Identify the blood parasite species.
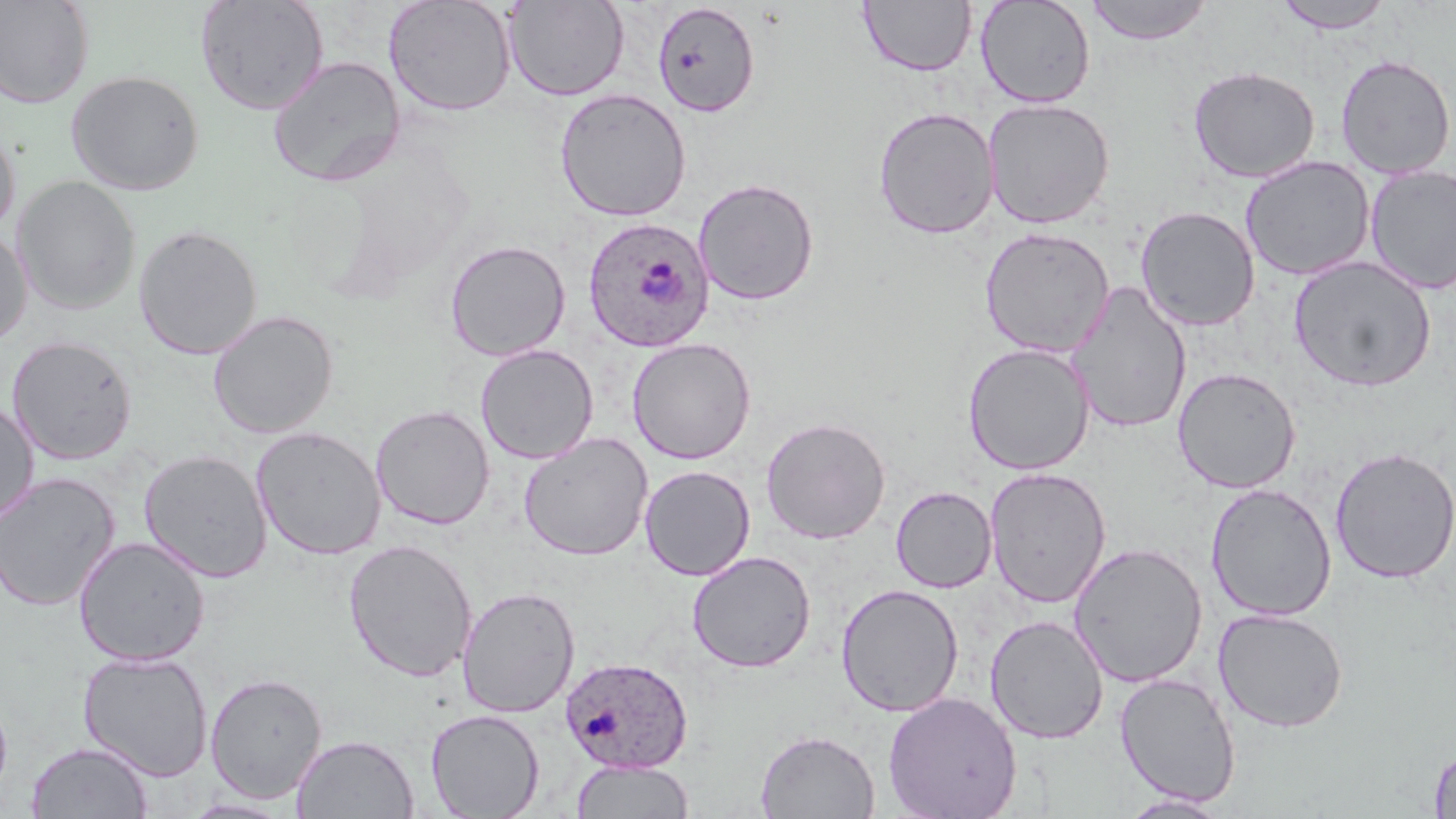
Plasmodium ovale.

Summary:
  - Coordinate format: approximate bounding boxes as (x1, y1, x2, y2) in pixels
  - Plasmodium ovale-infected red blood cell locations: (582, 216, 715, 352), (559, 655, 694, 773)
  - Uninfected red blood cell locations: (0, 0, 95, 109), (195, 0, 329, 115), (384, 0, 516, 118), (976, 0, 1096, 108), (1085, 0, 1214, 45), (505, 1, 629, 101), (859, 1, 977, 76), (1273, 1, 1395, 34), (651, 3, 761, 117), (1335, 54, 1455, 179), (268, 55, 407, 187), (1188, 64, 1321, 183), (66, 70, 205, 196), (554, 88, 692, 222), (982, 97, 1115, 229), (873, 106, 999, 239), (0, 124, 20, 239), (1239, 156, 1375, 281), (1365, 165, 1456, 294), (12, 175, 141, 315), (694, 178, 820, 306), (1135, 205, 1260, 331), (133, 224, 264, 360), (0, 226, 33, 349), (979, 227, 1115, 358), (444, 240, 571, 362), (1289, 255, 1437, 393), (1067, 281, 1193, 435), (207, 309, 339, 439), (6, 335, 138, 465), (627, 337, 757, 464), (962, 343, 1095, 476), (475, 344, 598, 464), (1172, 367, 1301, 494), (0, 401, 39, 527), (370, 404, 495, 529), (760, 416, 891, 544), (252, 426, 386, 560), (519, 432, 653, 561), (1330, 446, 1456, 583), (138, 449, 273, 583), (640, 465, 755, 581), (984, 467, 1111, 609), (0, 472, 120, 612), (1205, 483, 1337, 621), (890, 486, 997, 593), (73, 536, 210, 667), (343, 538, 478, 682), (1069, 541, 1208, 687), (687, 550, 816, 673), (836, 583, 964, 717), (458, 585, 580, 718), (1212, 606, 1349, 733), (985, 615, 1109, 744), (77, 650, 214, 782), (205, 672, 328, 804), (1114, 672, 1241, 807), (0, 686, 13, 807), (882, 691, 1022, 819), (426, 708, 545, 819), (756, 728, 880, 818), (291, 734, 419, 818), (26, 740, 153, 818), (1429, 745, 1456, 818), (571, 759, 694, 818), (1118, 793, 1232, 818), (181, 797, 296, 818)
  - Image size: 1456×819 pixels
  - Stain: May-Grünwald-Giemsa
  - Preparation: thin blood smear
  - Field of view: one of a larger specimen
  - Modality: optical microscopy
  - Magnification: 1000x